Assess this cell for malaria.
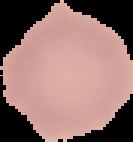

Uninfected.

Summary:
  - Image size: 133×142 pixels
  - Image type: segmented cell region on a black background
  - Preparation: thin blood smear